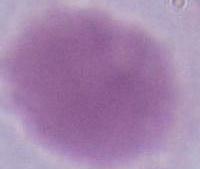 Photomicrograph. 1000x magnification. An erythrocyte is shown.